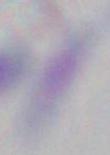 Captured at 1000x magnification. Micrograph. Toxoplasma gondii is shown.